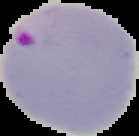 From a thin blood film. Malaria status: parasitized. Image is 139×136 pixels. The area outside the segmented cell region is set to black.